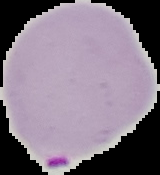
Summary:
  - Preparation: thin blood film
  - Image size: 160×175 pixels
  - Result: Plasmodium parasites detected
  - Image type: segmented cell region with the area outside set to black